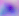

Summary:
  - Magnification: 400x
  - Identification: Toxoplasma gondii
  - Modality: micrograph